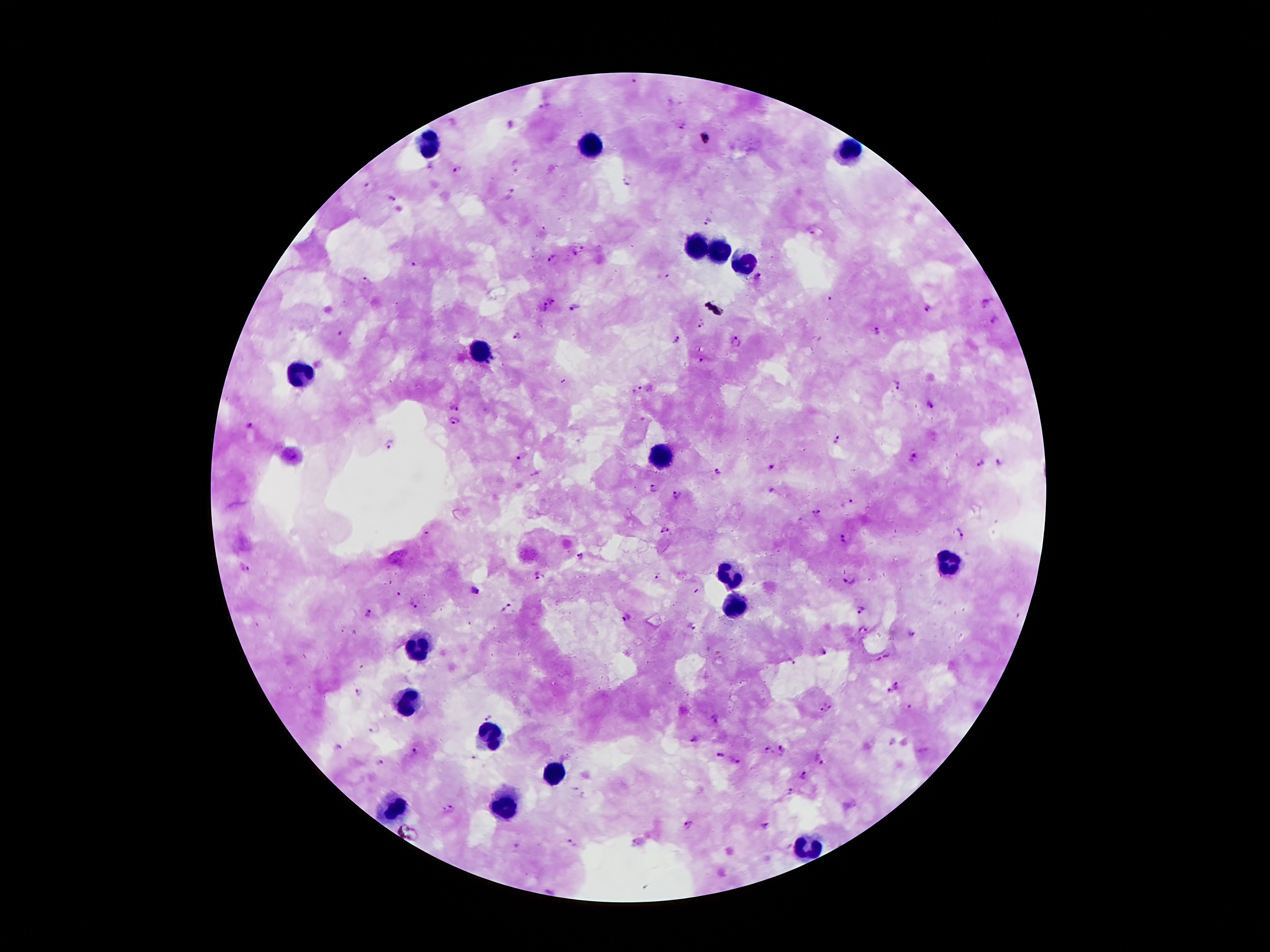
Approximate centers as [x, y] in pixels.
Summary:
  - Leukocyte locations: [429, 144], [592, 145], [847, 152], [701, 247], [719, 249], [744, 263], [479, 353], [304, 372], [661, 453], [946, 565], [733, 574], [733, 603], [420, 649], [409, 703], [490, 738], [554, 774], [506, 805], [393, 808], [806, 847]
  - Plasmodium parasite locations: [545, 105], [682, 127], [515, 165], [456, 169], [628, 181], [366, 184], [511, 192], [391, 198], [709, 221], [810, 230], [579, 251], [552, 259], [416, 264], [759, 277], [366, 280], [553, 300], [985, 301], [544, 308], [574, 308], [928, 309], [994, 321], [701, 325], [340, 333], [878, 334], [518, 336], [677, 339], [737, 342], [700, 359], [897, 385], [637, 389], [928, 403], [454, 407], [453, 419], [248, 427], [836, 439], [387, 444], [524, 457], [914, 457], [981, 464], [999, 464], [771, 467], [716, 471], [650, 489], [773, 491], [677, 494], [851, 501], [816, 513], [665, 529], [960, 535], [845, 539], [582, 557], [245, 568], [658, 575], [538, 576], [851, 580], [475, 590], [397, 594], [413, 605], [507, 607], [862, 611], [368, 613], [627, 618], [693, 627], [910, 634], [825, 653], [791, 662], [897, 685], [890, 690], [359, 693], [908, 707], [826, 709], [489, 717], [716, 717], [374, 727], [696, 740], [338, 746], [767, 751], [784, 751], [413, 753], [720, 755], [474, 757], [380, 762], [738, 763], [822, 763], [803, 776], [574, 788], [791, 793], [582, 795], [451, 810], [687, 825], [767, 826], [571, 843], [517, 846]
  - Preparation: thick blood film
  - Magnification: 100x
  - Stain: Giemsa
  - Image size: 1270×952 pixels
  - Capture: smartphone camera through the microscope eyepiece
  - Patient malaria status: infected with Plasmodium falciparum
  - Field of view: one from this slide